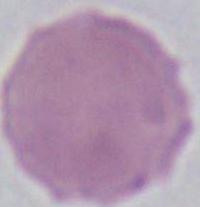
1000x magnification. Photomicrograph. A red blood cell is seen.